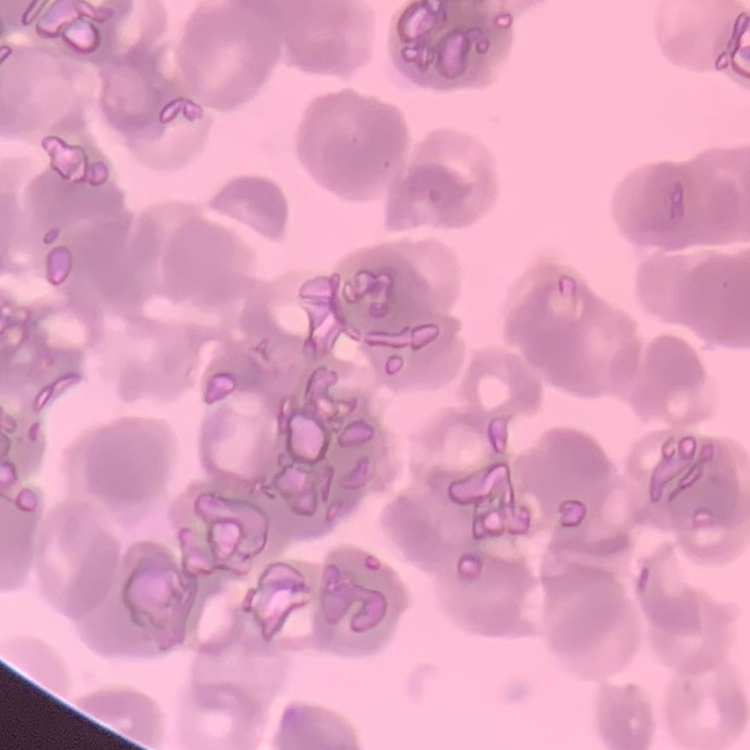

red blood cell morphology = rouleaux formation
stain = Field's or Giemsa
image type = square crop of a larger photomicrograph
preparation = thin blood smear